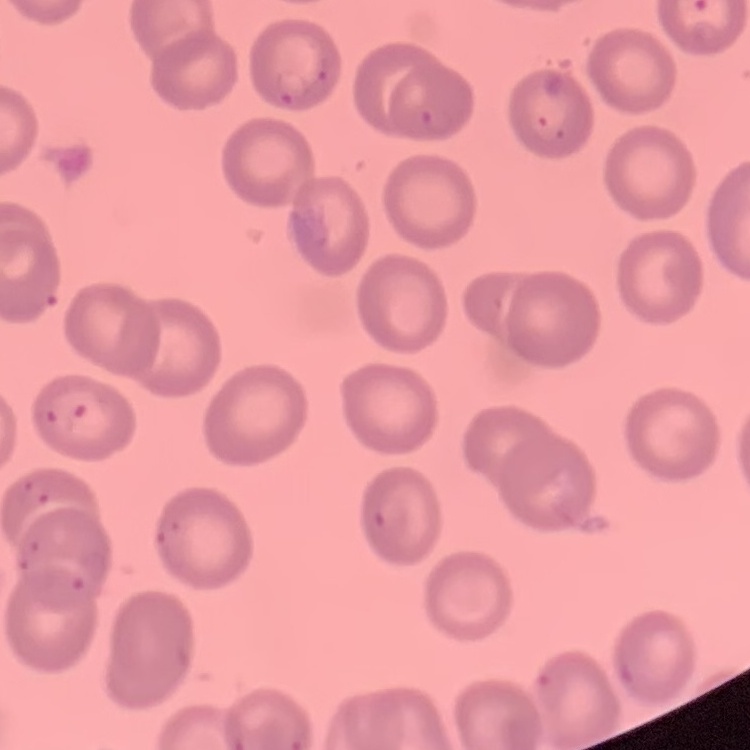
erythrocyte_morphology: no rouleaux formation
preparation: thin blood film
image_type: one tile cut from a larger photomicrograph
stain: Field's or Giemsa